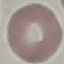

Malaria status: uninfected. Photographed with a smartphone camera at the microscope eyepiece. Thin blood film. Automatically extracted cell patch, resized to 64 × 64 pixels. Giemsa-stained preparation.